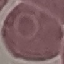

Summary:
  - Malaria status: uninfected
  - Image type: cell patch, automatically extracted from a larger field of view and resized to 64 × 64 pixels
  - Stain: Giemsa
  - Capture: smartphone camera at the microscope eyepiece
  - Preparation: thin smear